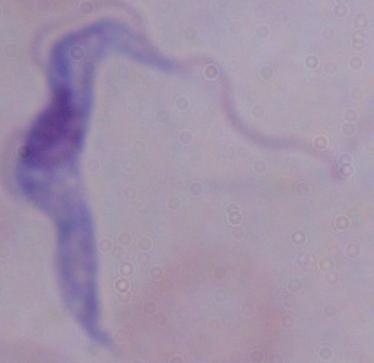

Summary:
  - Identification: trypanosome
  - Modality: micrograph
  - Magnification: 1000x